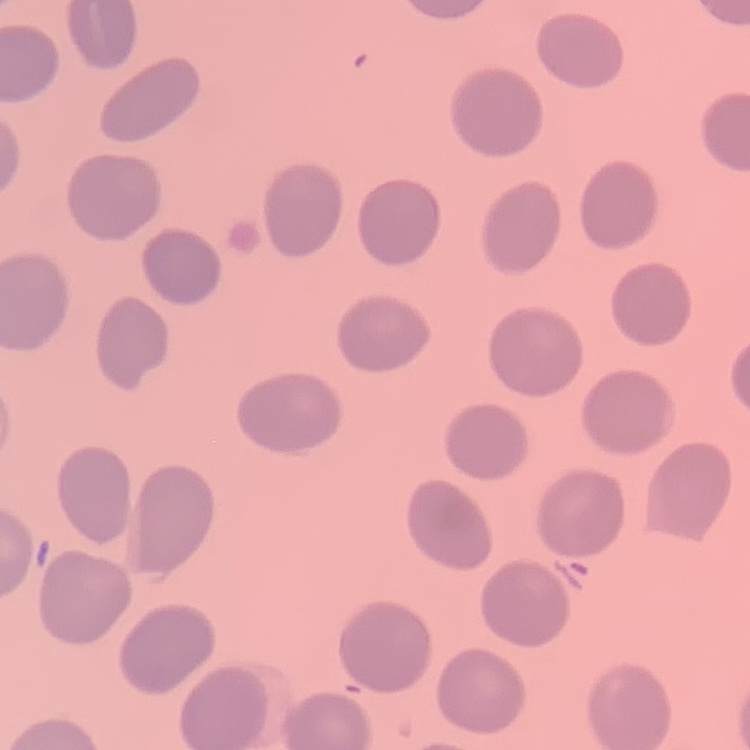
red blood cell morphology = no rouleaux formation
stain = Field's or Giemsa
image type = one tile cut from a larger photomicrograph
preparation = thin blood smear